State the blood parasite species.
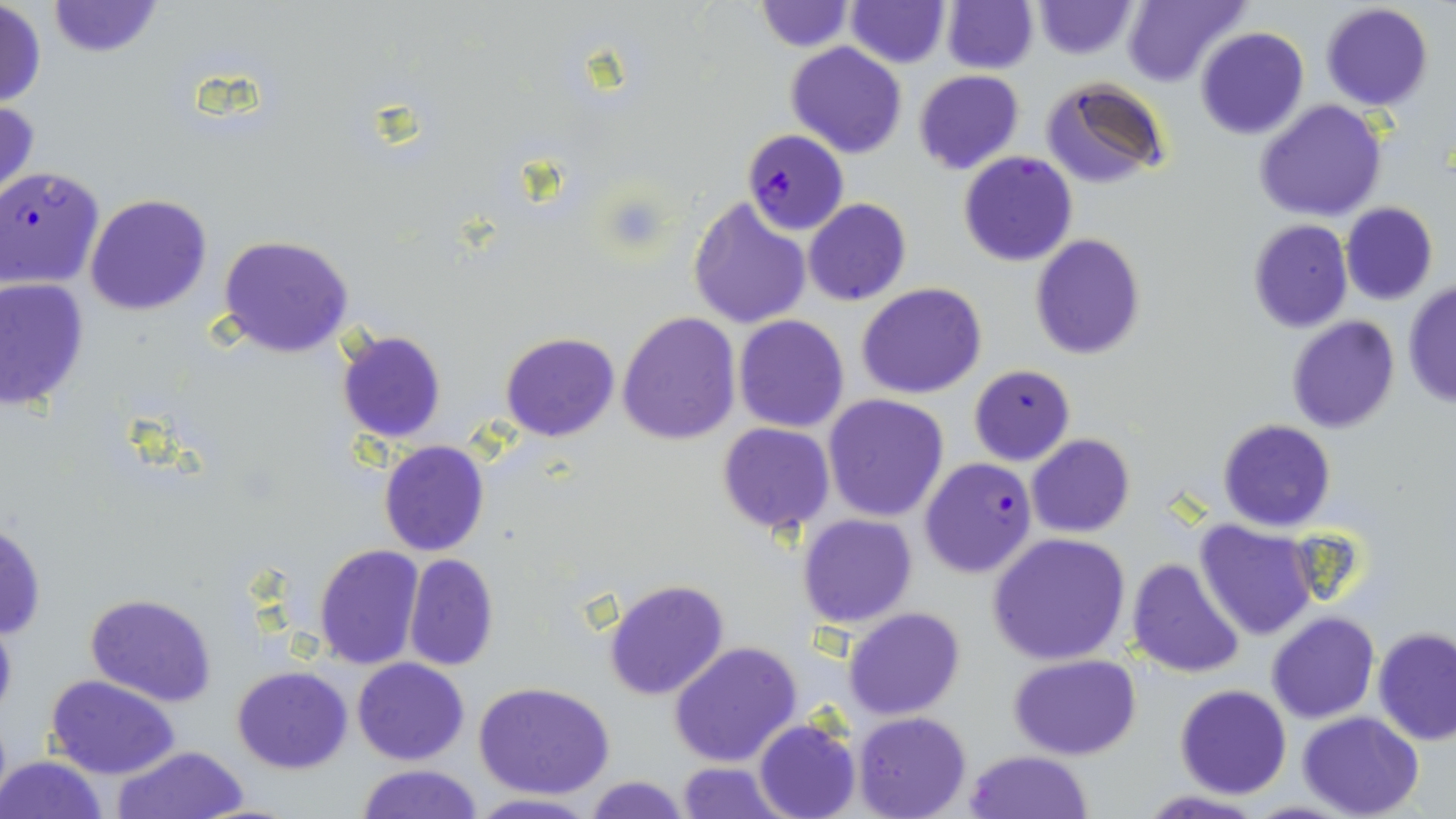
Plasmodium falciparum.

stain = May-Grünwald-Giemsa
Plasmodium falciparum-infected red blood cell locations = approximate bounding boxes as named x1/y1/x2/y2 corners in pixels: (x1=741, y1=130, x2=848, y2=235), (x1=0, y1=167, x2=104, y2=287), (x1=919, y1=457, x2=1037, y2=578)
uninfected red blood cell locations = approximate bounding boxes as named x1/y1/x2/y2 corners in pixels: (x1=45, y1=0, x2=163, y2=57), (x1=754, y1=1, x2=852, y2=52), (x1=942, y1=1, x2=1037, y2=73), (x1=1030, y1=1, x2=1140, y2=59), (x1=1122, y1=1, x2=1250, y2=86), (x1=846, y1=2, x2=950, y2=67), (x1=0, y1=3, x2=46, y2=107), (x1=1320, y1=3, x2=1433, y2=112), (x1=1195, y1=26, x2=1309, y2=139), (x1=785, y1=41, x2=907, y2=159), (x1=913, y1=70, x2=1024, y2=174), (x1=1042, y1=77, x2=1171, y2=189), (x1=0, y1=97, x2=39, y2=205), (x1=1253, y1=99, x2=1389, y2=222), (x1=958, y1=151, x2=1078, y2=267), (x1=85, y1=193, x2=213, y2=316), (x1=687, y1=196, x2=813, y2=330), (x1=803, y1=198, x2=912, y2=306), (x1=1341, y1=203, x2=1439, y2=304), (x1=1248, y1=219, x2=1354, y2=333), (x1=1030, y1=234, x2=1145, y2=359), (x1=219, y1=235, x2=354, y2=357), (x1=0, y1=277, x2=90, y2=410), (x1=858, y1=282, x2=987, y2=400), (x1=1403, y1=282, x2=1455, y2=408), (x1=618, y1=311, x2=741, y2=445), (x1=734, y1=315, x2=850, y2=434), (x1=1286, y1=316, x2=1400, y2=435), (x1=335, y1=329, x2=447, y2=444), (x1=500, y1=333, x2=620, y2=441), (x1=969, y1=364, x2=1075, y2=466), (x1=823, y1=394, x2=949, y2=522), (x1=1218, y1=420, x2=1336, y2=532), (x1=717, y1=423, x2=835, y2=533), (x1=1027, y1=434, x2=1134, y2=539), (x1=378, y1=440, x2=490, y2=557), (x1=797, y1=514, x2=918, y2=629), (x1=0, y1=518, x2=47, y2=641), (x1=1194, y1=520, x2=1318, y2=640), (x1=988, y1=532, x2=1133, y2=666), (x1=314, y1=545, x2=423, y2=668), (x1=404, y1=554, x2=498, y2=671), (x1=1126, y1=557, x2=1246, y2=678), (x1=601, y1=576, x2=730, y2=701), (x1=84, y1=592, x2=217, y2=707), (x1=843, y1=607, x2=965, y2=720), (x1=1265, y1=612, x2=1379, y2=724), (x1=0, y1=616, x2=17, y2=724), (x1=1372, y1=628, x2=1456, y2=746), (x1=669, y1=641, x2=803, y2=769), (x1=1009, y1=652, x2=1141, y2=759), (x1=352, y1=657, x2=470, y2=765), (x1=231, y1=665, x2=353, y2=774), (x1=45, y1=674, x2=181, y2=780), (x1=474, y1=681, x2=618, y2=800), (x1=1175, y1=684, x2=1292, y2=799), (x1=1298, y1=712, x2=1423, y2=819), (x1=853, y1=713, x2=970, y2=819), (x1=753, y1=719, x2=862, y2=819), (x1=112, y1=745, x2=248, y2=819), (x1=964, y1=751, x2=1091, y2=818), (x1=1, y1=754, x2=110, y2=819), (x1=674, y1=761, x2=790, y2=819), (x1=354, y1=763, x2=484, y2=819), (x1=584, y1=776, x2=691, y2=818), (x1=1134, y1=791, x2=1270, y2=819), (x1=466, y1=792, x2=598, y2=818)
preparation = thin blood film
field of view = one of a larger specimen
modality = optical microscopy
image size = 1456×819 pixels
magnification = 1000x